Assess this cell for malaria.
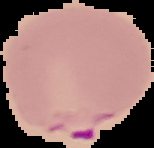

Parasitized.

Image is 154×148 pixels. The area outside the segmented cell region is set to black. From a thin blood smear.